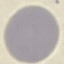

Malaria status: uninfected. Giemsa-stained preparation. Automatically extracted cell patch, resized to 64 × 64 pixels. Thin smear of blood. Acquired by smartphone through the microscope eyepiece.